Describe the morphology of the red blood cells.
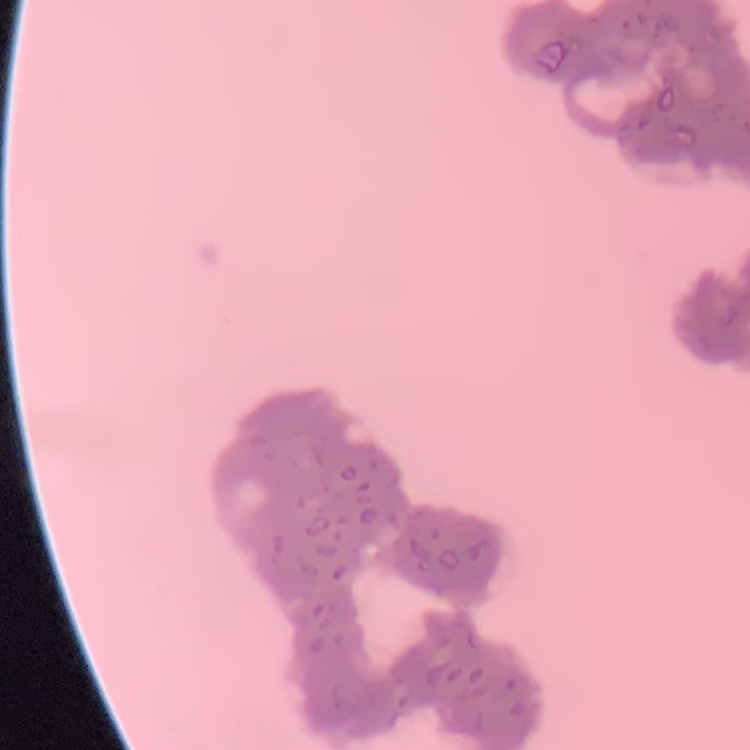

Rouleaux formation.

Square crop of a larger photomicrograph. Field's or Giemsa stain. Thin blood film.